Comment on the morphology of the erythrocytes.
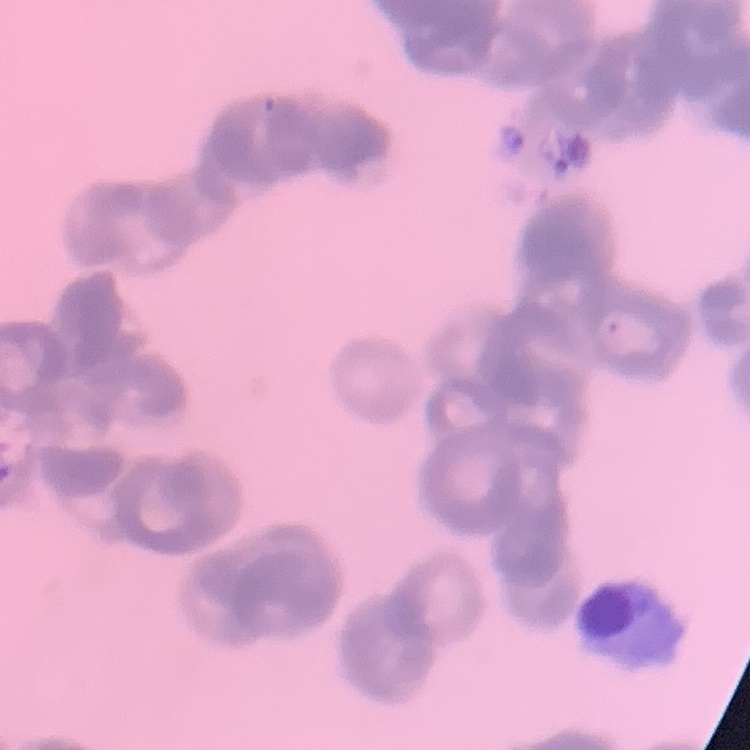

They show rouleaux formation.

Summary:
  - Preparation: thin blood smear
  - Stain: Field's or Giemsa
  - Image type: square crop of a larger photomicrograph